State which parasite is depicted.
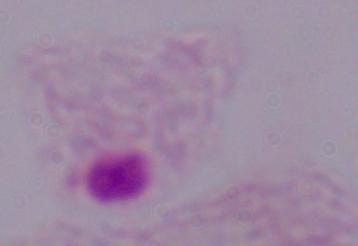

A trichomonad.

magnification = 1000x
modality = micrograph